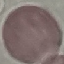 Malaria status: uninfected. Automatically extracted cell patch, resized to 64 × 64 pixels. Thin blood film. Giemsa-stained preparation. Photographed with a smartphone camera at the microscope eyepiece.